Classify this cell by malaria status.
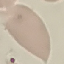
Uninfected.

Giemsa stain. Photographed with a smartphone camera at the microscope eyepiece. Thin smear of blood. Cell patch, automatically extracted from a larger field of view and resized to 64 × 64 pixels.